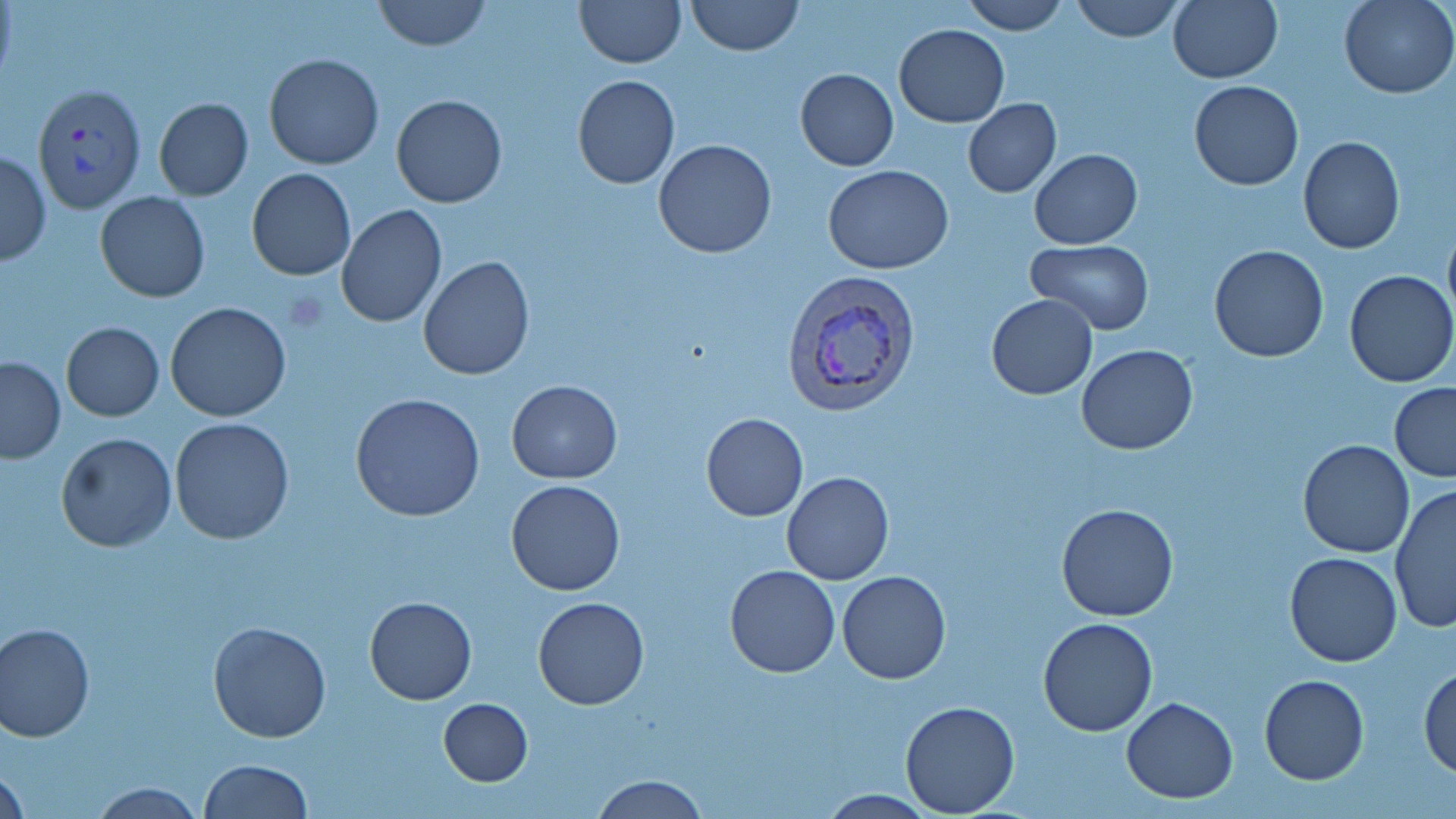

slide_level_diagnosis: Plasmodium vivax
modality: light microscopy
magnification: 1000x
field_of_view: single
uninfected_red_blood_cell_locations: 'approximate bounding boxes as (x1, y1, x2, y2) in pixels: (373, 0, 490, 51), (575, 0, 686, 68), (685, 0, 803, 55), (960, 0, 1071, 35), (1069, 0, 1185, 43), (1169, 0, 1282, 83), (1339, 0, 1455, 98), (893, 24, 1009, 128), (263, 54, 384, 170), (794, 68, 900, 171), (572, 75, 680, 189), (1189, 81, 1303, 190), (390, 94, 508, 208), (153, 98, 253, 201), (962, 100, 1062, 197), (1297, 137, 1405, 255), (652, 138, 778, 258), (1029, 149, 1142, 248), (1, 150, 51, 265), (824, 166, 951, 275), (246, 168, 357, 280), (94, 192, 210, 303), (336, 205, 448, 330), (1442, 218, 1456, 334), (1026, 240, 1154, 334), (1209, 245, 1329, 363), (418, 255, 535, 380), (1344, 270, 1456, 387), (985, 294, 1098, 400), (165, 302, 291, 421), (62, 322, 164, 421), (1076, 344, 1199, 454), (0, 356, 64, 462), (506, 380, 623, 484), (1389, 383, 1456, 483), (351, 392, 485, 522), (700, 412, 808, 522), (169, 417, 296, 544), (56, 432, 177, 551), (1297, 439, 1415, 557), (783, 471, 893, 586), (506, 478, 625, 596), (1390, 484, 1455, 632), (1056, 502, 1180, 622), (1283, 552, 1403, 667), (724, 566, 841, 678), (837, 570, 951, 684), (365, 595, 477, 705), (533, 596, 649, 710), (1037, 617, 1158, 737), (207, 620, 332, 742), (0, 622, 97, 742), (1418, 662, 1456, 779), (1259, 676, 1369, 785), (1121, 696, 1238, 803), (438, 698, 533, 785), (899, 700, 1020, 815), (198, 759, 314, 818), (2, 763, 28, 819), (590, 774, 708, 818), (87, 781, 207, 818), (813, 789, 940, 817)'
image_size: 1456×819 pixels
stain: May-Grünwald-Giemsa
plasmodium_vivax_infected_red_blood_cell_locations: 'approximate bounding boxes as (x1, y1, x2, y2) in pixels: (36, 83, 149, 212), (784, 271, 920, 414)'
preparation: thin blood smear